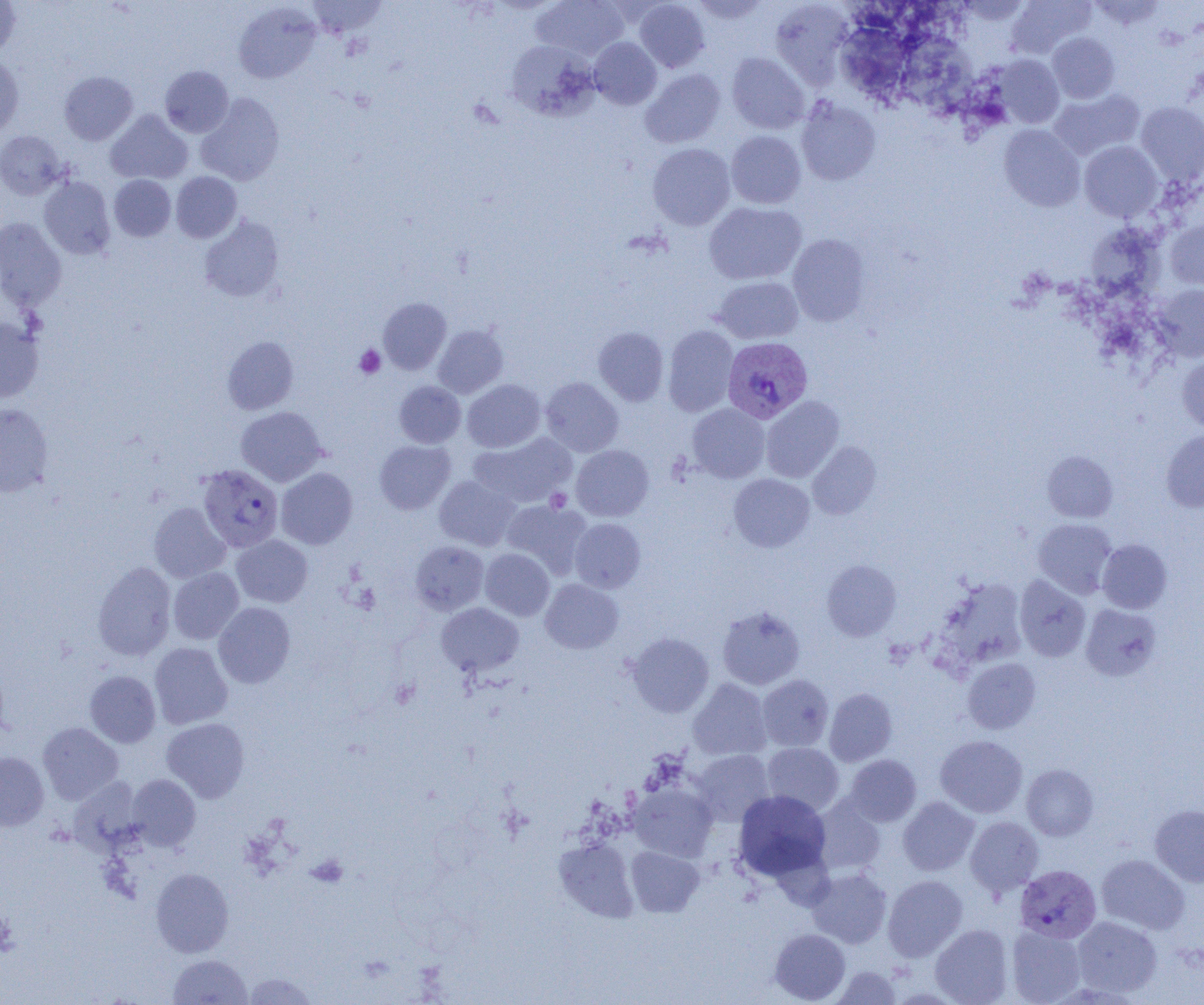

Approximate bounding boxes as [x1, y1, x2, y2] in pixels. Platelet locations: [354, 345, 385, 378], [545, 488, 572, 512], [307, 854, 348, 888]. Plasmodium vivax-infected red blood cell locations: [722, 337, 812, 423], [198, 464, 283, 552], [1015, 864, 1101, 943]. Uninfected red blood cell locations: [0, 0, 21, 56], [307, 0, 386, 38], [532, 0, 628, 61], [634, 0, 710, 72], [1008, 0, 1095, 58], [1088, 0, 1166, 30], [691, 1, 771, 24], [770, 1, 854, 87], [234, 2, 321, 84], [840, 26, 913, 98], [902, 29, 980, 112], [1047, 32, 1119, 103], [589, 37, 662, 110], [506, 40, 599, 120], [727, 52, 809, 134], [993, 54, 1064, 128], [0, 55, 24, 138], [160, 66, 233, 137], [640, 68, 725, 148], [59, 71, 138, 145], [1048, 88, 1144, 160], [196, 93, 284, 186], [796, 97, 881, 185], [1136, 102, 1204, 185], [105, 110, 193, 184], [999, 125, 1085, 211], [0, 130, 67, 199], [726, 131, 806, 209], [1080, 140, 1163, 221], [648, 143, 735, 230], [171, 172, 241, 242], [109, 175, 176, 241], [39, 177, 116, 259], [704, 202, 806, 285], [199, 216, 284, 302], [1165, 217, 1204, 289], [0, 218, 66, 310], [787, 234, 871, 326], [713, 276, 804, 344], [1151, 284, 1204, 361], [378, 298, 451, 374], [0, 317, 44, 402], [433, 325, 508, 397], [663, 325, 738, 416], [593, 327, 669, 406], [222, 336, 299, 415], [1177, 355, 1204, 432], [541, 377, 623, 456], [462, 379, 545, 452], [394, 381, 466, 448], [761, 395, 844, 482], [0, 404, 53, 496], [687, 404, 769, 482], [236, 406, 326, 486], [1161, 429, 1204, 512], [470, 433, 576, 509], [374, 440, 455, 514], [807, 442, 881, 519], [571, 445, 654, 521], [1042, 451, 1118, 522], [276, 467, 358, 549], [728, 473, 814, 552], [435, 475, 520, 551], [501, 500, 592, 576], [149, 502, 230, 583], [569, 517, 646, 592], [1033, 518, 1117, 599], [231, 535, 313, 607], [1097, 540, 1172, 613], [411, 541, 488, 614], [480, 548, 554, 621], [822, 560, 901, 640], [92, 562, 176, 661], [168, 568, 244, 644], [1014, 575, 1091, 662], [938, 577, 1028, 668], [540, 579, 623, 654], [213, 602, 295, 687], [436, 602, 524, 677], [1080, 603, 1162, 681], [718, 606, 805, 690], [626, 633, 713, 717], [149, 642, 232, 729], [962, 658, 1040, 734], [85, 670, 161, 747], [758, 674, 833, 751], [688, 678, 772, 760], [824, 688, 897, 766], [162, 717, 249, 802], [38, 722, 123, 804], [935, 735, 1027, 818], [762, 743, 844, 815], [690, 750, 774, 825], [0, 752, 49, 831], [845, 754, 921, 826], [1021, 764, 1098, 840], [128, 774, 200, 850], [68, 777, 144, 853], [628, 782, 718, 862], [733, 790, 831, 881], [813, 797, 886, 876], [898, 797, 979, 875], [1150, 804, 1204, 887], [964, 816, 1044, 897], [554, 838, 638, 921], [626, 846, 704, 917], [1096, 854, 1190, 935], [151, 868, 233, 957], [806, 868, 892, 948], [883, 874, 968, 961], [1072, 916, 1163, 997], [930, 924, 1013, 1004], [1006, 924, 1087, 1004], [770, 928, 850, 1003], [168, 954, 252, 1004], [831, 965, 902, 1004], [243, 972, 317, 1005]. Slide-level diagnosis: Plasmodium vivax. Thin blood smear. Light microscopy. One field of a larger specimen. Image is 1204×1005 pixels. 1000x magnification.